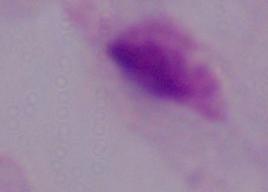

Summary:
  - Identification: trichomonad
  - Magnification: 1000x
  - Modality: photomicrograph